Classify this cell by malaria status.
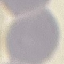
Uninfected.

Summary:
  - Stain: Giemsa
  - Preparation: thin blood film
  - Capture: smartphone through the microscope eyepiece
  - Image type: cell patch, automatically extracted from a larger field of view and resized to 64 × 64 pixels